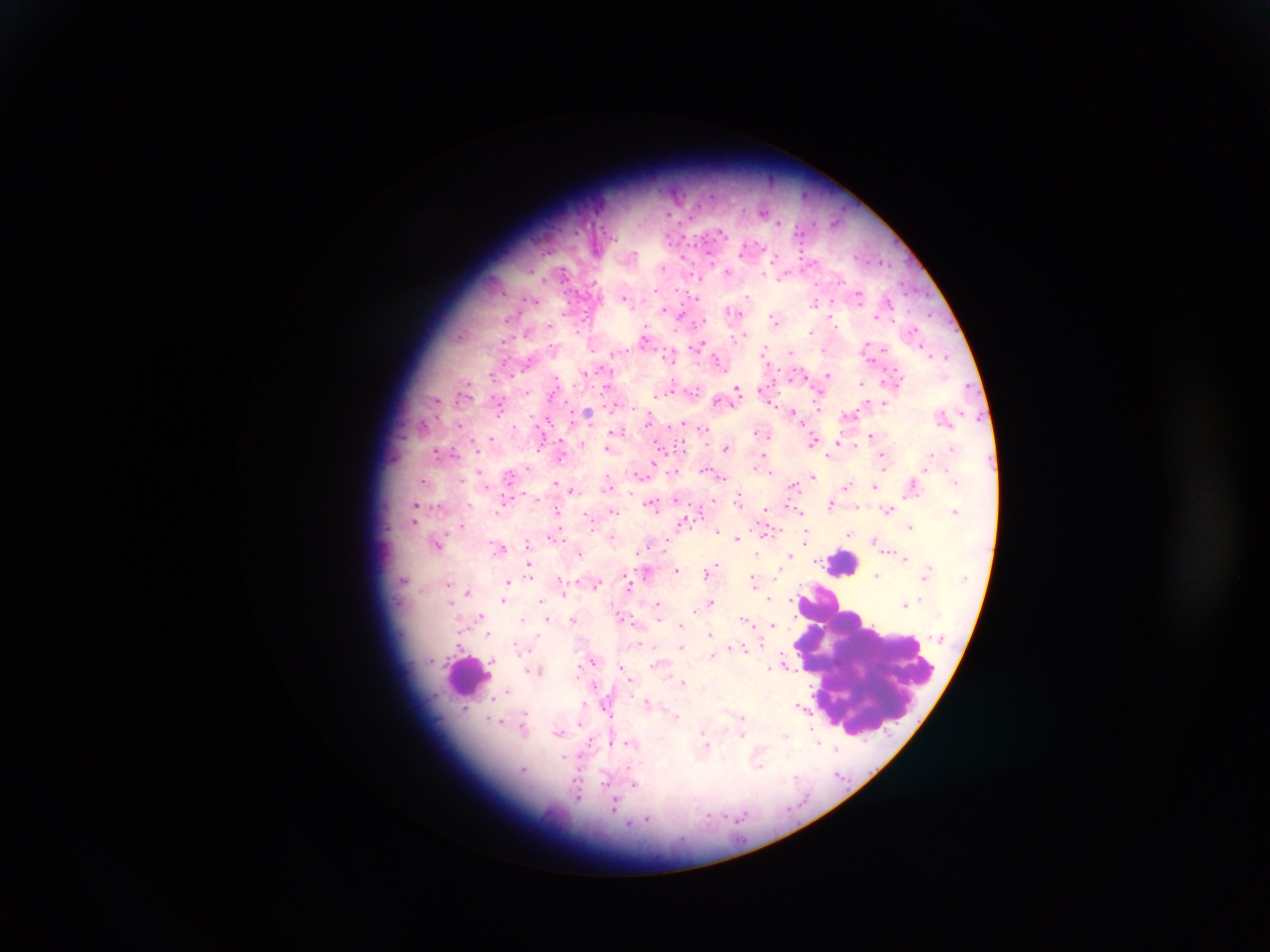
Approximate centers as x y in pixels.
Summary:
  - Leukocyte locations: 844 563; 868 664; 468 675
  - Malaria parasite locations: 764 210; 779 222; 729 271; 858 293; 624 296; 748 296; 534 300; 815 302; 666 310; 732 311; 679 312; 832 316; 877 316; 776 319; 700 321; 812 331; 645 336; 738 337; 869 345; 923 345; 699 346; 790 352; 616 354; 669 355; 947 355; 766 356; 717 360; 585 373; 492 375; 803 375; 828 375; 789 376; 862 383; 607 385; 737 389; 762 389; 693 390; 671 391; 465 394; 655 394; 436 399; 717 400; 499 403; 884 403; 616 405; 819 407; 792 411; 587 414; 850 415; 649 420; 544 422; 684 423; 459 424; 514 427; 703 429; 619 430; 759 432; 872 435; 491 439; 813 441; 837 441; 475 442; 583 443; 561 444; 661 445; 608 448; 726 448; 440 452; 766 455; 561 456; 884 456; 653 464; 527 467; 756 467; 480 470; 675 471; 770 471; 639 474; 773 474; 720 476; 813 476; 509 478; 462 479; 424 481; 555 482; 609 482; 793 484; 874 484; 847 485; 913 486; 572 490; 632 493; 676 498; 739 499; 505 501; 832 502; 652 503; 417 504; 502 504; 794 507; 417 509; 765 509; 888 509; 558 510; 955 510; 613 511; 589 517; 684 520; 417 521; 910 526; 462 527; 717 529; 765 532; 850 534; 555 535; 806 535; 612 537; 736 537; 668 540; 875 541; 437 543; 529 543; 645 547; 502 548; 580 552; 758 553; 790 555; 906 558; 529 565; 718 565; 677 570; 708 572; 646 573; 877 574; 403 579; 560 579; 753 580; 508 581; 448 582; 629 583; 597 584; 563 585; 468 591; 564 591; 770 598; 791 598; 451 600; 504 600; 542 600; 711 600; 658 604; 905 604; 697 611; 481 615; 523 618; 547 618; 574 619; 747 620; 681 623; 774 624; 488 632; 710 633; 639 643; 460 645; 681 647; 744 647; 521 650; 712 653; 592 660; 661 662; 786 664; 623 669; 539 671; 684 682; 595 686; 649 704; 584 705; 465 707; 804 708; 742 719; 492 721; 522 728; 742 731; 559 733; 785 735; 592 741; 818 742; 707 744; 836 749; 635 783; 614 805
  - Field of view: single
  - Country: Ghana
  - Preparation: thick blood smear
  - Image size: 1270×952 pixels
  - Capture: mobile-phone photograph through a microscope